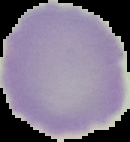
result: no Plasmodium parasites detected
image_size: 130×142 pixels
preparation: thin blood film
image_type: segmented cell region on a black background